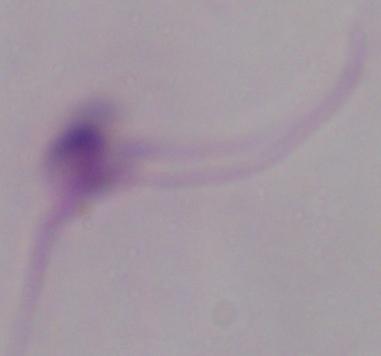

magnification = 1000x
modality = photomicrograph
identification = Leishmania